Assess the morphology of the erythrocytes.
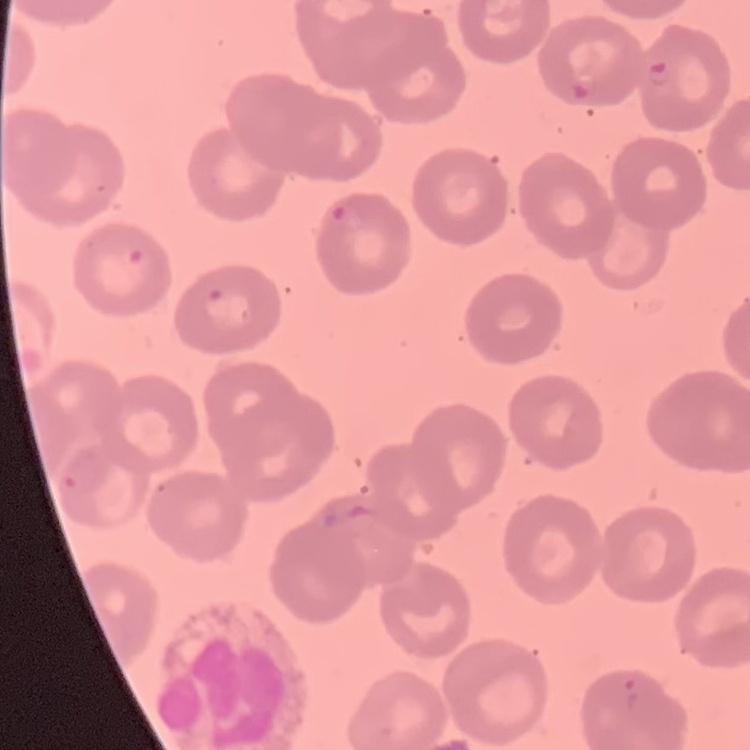

No rouleaux formation.

Summary:
  - Image type: one tile cut from a larger photomicrograph
  - Preparation: thin peripheral smear
  - Stain: Field's or Giemsa